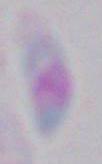

magnification: 1000x
modality: micrograph
identification: Toxoplasma gondii